Give the position of every Plasmodium parasite visible.
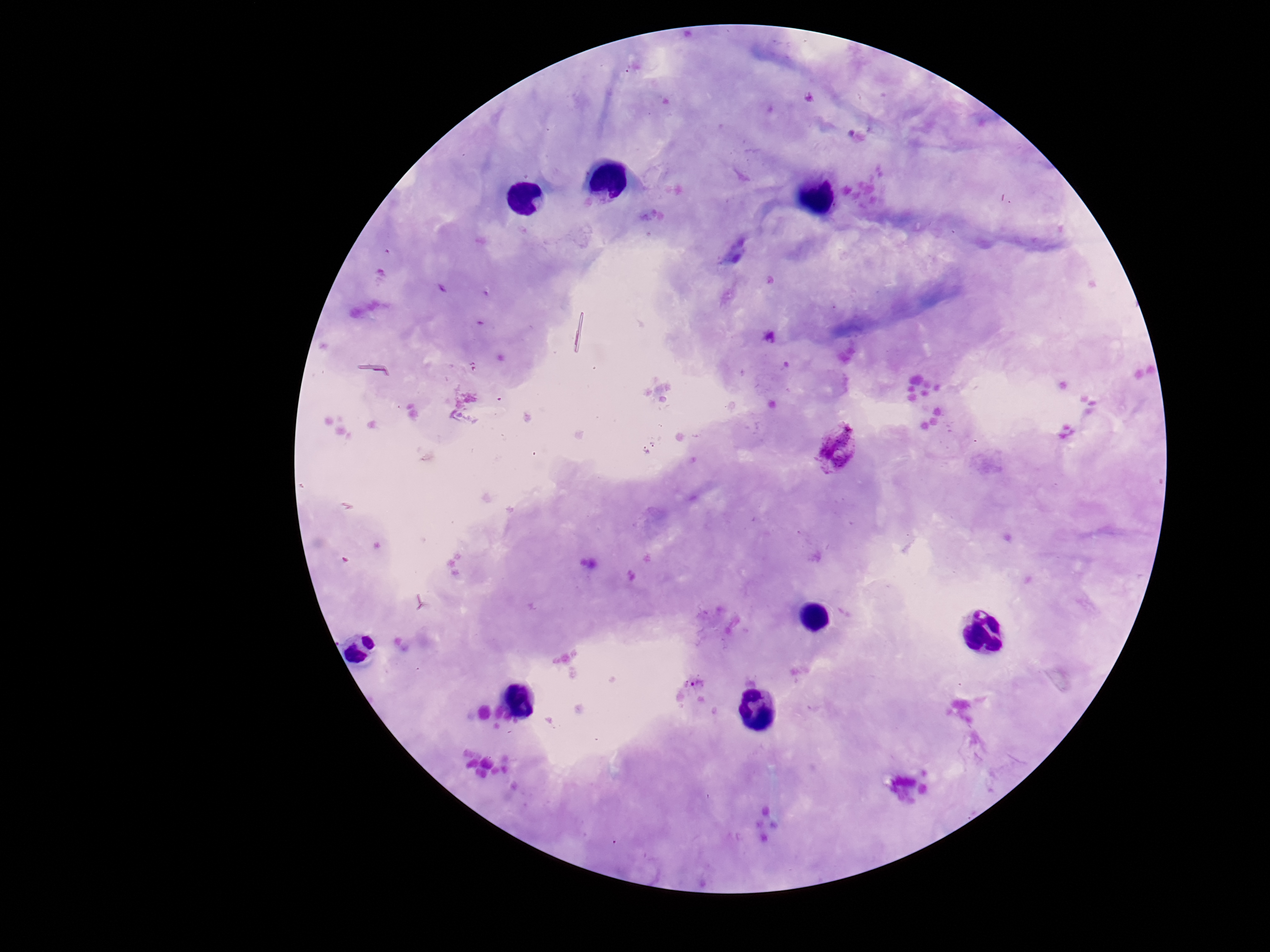
Approximate centers as [x, y] in pixels.
Plasmodium parasites: [837, 447], [695, 684].

{
  "capture": "smartphone camera through the microscope eyepiece",
  "stain": "Giemsa",
  "field_of_view": "single",
  "preparation": "thick blood film",
  "patient_malaria_status": "positive",
  "image_size": "1270×952 pixels",
  "magnification": "100x"
}